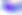 Captured at 400x magnification. Micrograph. Toxoplasma gondii is seen.